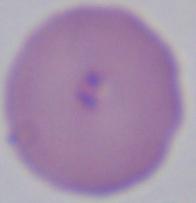

Captured at 1000x magnification. Micrograph. A Babesia parasite is seen.